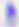
{
  "magnification": "400x",
  "identification": "Toxoplasma gondii",
  "modality": "photomicrograph"
}